State which parasite is depicted.
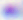

This is Toxoplasma gondii.

magnification: 400x
modality: photomicrograph